Comment on the morphology of the red blood cells.
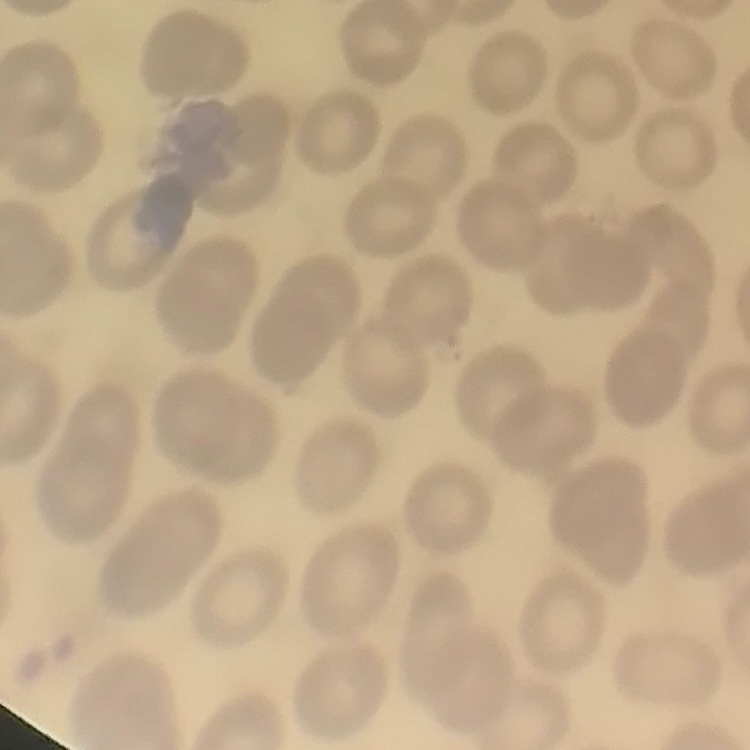
No rouleaux formation.

Thin blood film. Field's or Giemsa stain. Square crop of a larger photomicrograph.